Assess this cell for malaria.
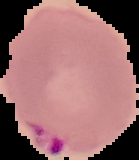
Parasitized.

image type = segmented cell region on a black background
image size = 139×160 pixels
preparation = thin blood smear